Classify this cell by malaria status.
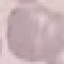
Uninfected.

Summary:
  - Stain: Giemsa
  - Preparation: thin blood film
  - Capture: smartphone camera at the microscope eyepiece
  - Image type: cell patch, automatically extracted from a larger field of view and resized to 64 × 64 pixels